Assess this cell for malaria.
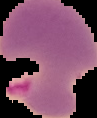
Parasitized.

Summary:
  - Image size: 97×118 pixels
  - Image type: cell region segmented out of the field of view; surrounding area masked to black
  - Preparation: thin blood smear